Point out each Plasmodium parasite.
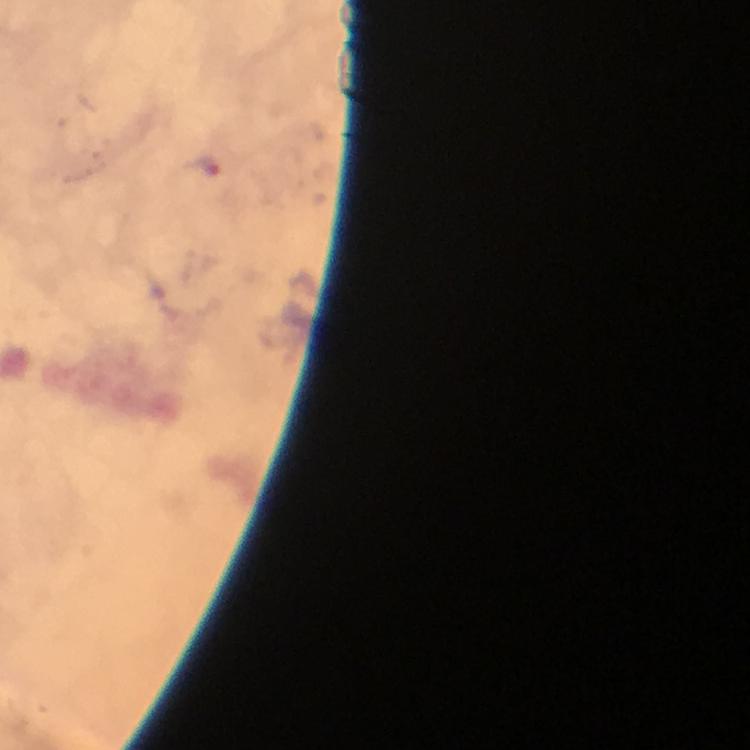

Approximate object centers, in pixels from the top-left corner.
Plasmodium parasites: (x=202, y=167).

{
  "preparation": "thick blood film",
  "immersion_oil": "applied",
  "image_size": "750×750 pixels",
  "cropped_from": "a single field of view",
  "context": "from a malaria diagnostic workup",
  "capture": "smartphone photograph through a microscope",
  "stain": "Giemsa",
  "magnification": "100x"
}